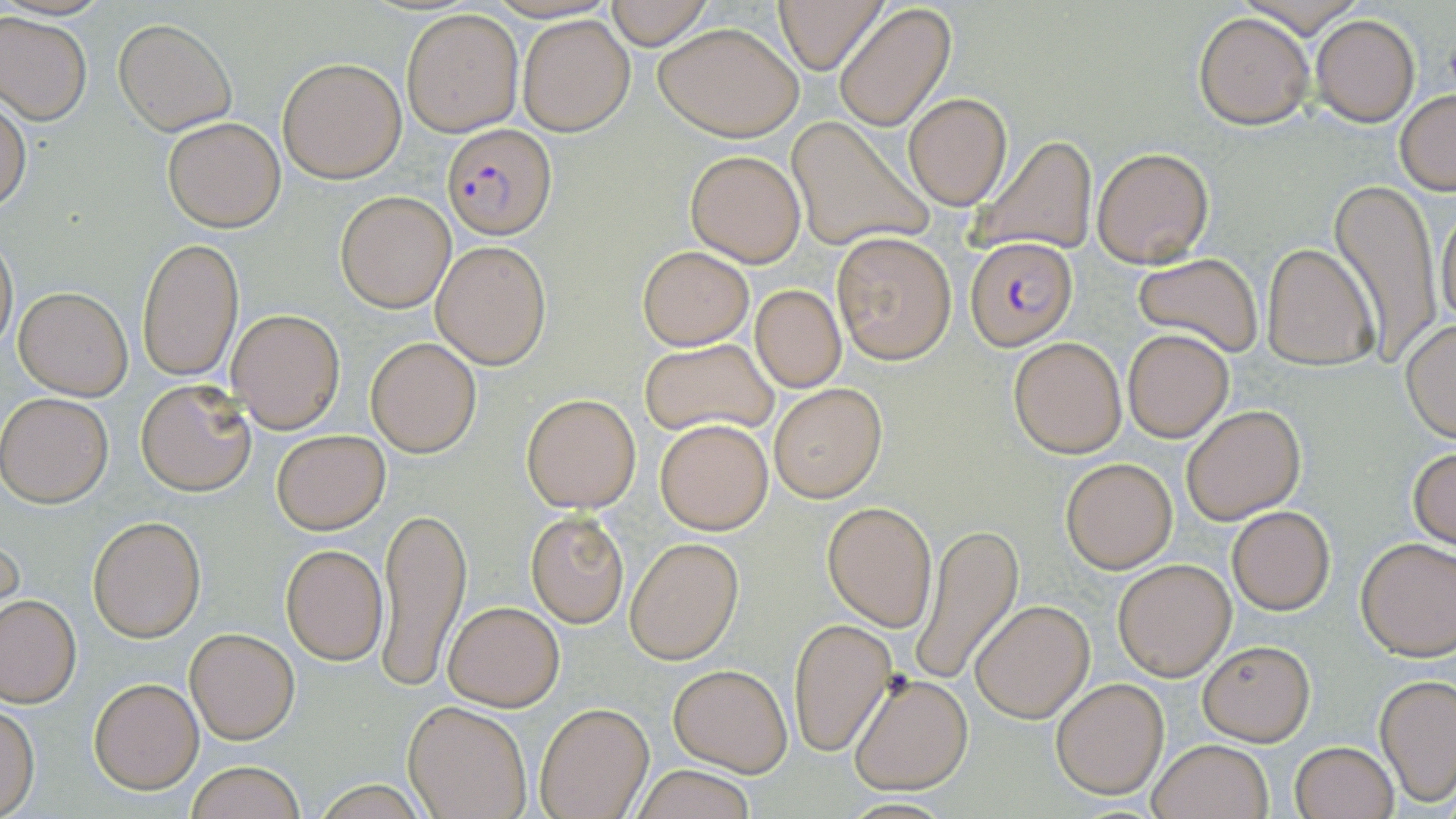
Approximate bounding boxes as (x1,y1)-(x2,y2) corner pairs in pixels. Uninfected red blood cell locations: (604,0)-(712,48), (775,0)-(885,73), (834,3)-(955,130), (402,8)-(526,137), (1192,11)-(1314,128), (0,12)-(92,124), (517,13)-(636,137), (1311,14)-(1420,126), (114,18)-(237,135), (654,22)-(803,141), (277,57)-(406,183), (0,91)-(30,214), (1396,91)-(1456,194), (904,93)-(1011,209), (805,102)-(1014,220), (163,117)-(285,232), (786,117)-(931,252), (968,133)-(1099,258), (1091,146)-(1214,267), (686,150)-(806,267), (1328,180)-(1444,362), (335,190)-(456,312), (1436,202)-(1456,336), (0,228)-(17,357), (831,231)-(957,365), (136,237)-(243,382), (432,239)-(551,368), (1260,242)-(1379,372), (638,246)-(752,349), (1131,252)-(1263,359), (13,285)-(134,399), (750,286)-(847,392), (225,309)-(345,432), (1399,320)-(1456,442), (1121,327)-(1234,442), (1007,336)-(1126,457), (366,337)-(481,457), (639,338)-(778,438), (135,379)-(254,495), (769,383)-(887,501), (1,392)-(113,506), (520,392)-(642,513), (1180,404)-(1306,524), (655,419)-(774,534), (271,429)-(390,534), (1409,446)-(1455,550), (1060,457)-(1178,573), (374,498)-(470,696), (822,500)-(938,633), (1225,504)-(1336,615), (526,511)-(629,628), (88,515)-(205,642), (909,524)-(1023,689), (0,525)-(22,627), (1355,536)-(1456,660), (625,538)-(743,664), (280,542)-(388,666), (1113,558)-(1235,680), (1,595)-(80,707), (442,600)-(564,710), (970,601)-(1094,722), (789,618)-(897,756), (185,627)-(299,744), (1196,638)-(1315,746), (669,663)-(792,776), (848,672)-(973,794), (1376,674)-(1454,806), (1051,677)-(1169,798), (89,678)-(203,793), (404,701)-(532,819), (535,701)-(653,819), (0,704)-(39,817), (1147,738)-(1274,819), (1288,741)-(1398,819), (184,760)-(308,819), (632,765)-(759,819). Plasmodium falciparum-infected red blood cell locations: (443,122)-(556,240), (964,236)-(1077,350). Slide-level diagnosis: Plasmodium falciparum. Thin blood smear. Image is 1456×819 pixels. May-Grünwald-Giemsa-stained preparation. Optical microscopy. One field of a larger specimen. Captured at 1000x magnification.